Comment on the morphology of the erythrocytes.
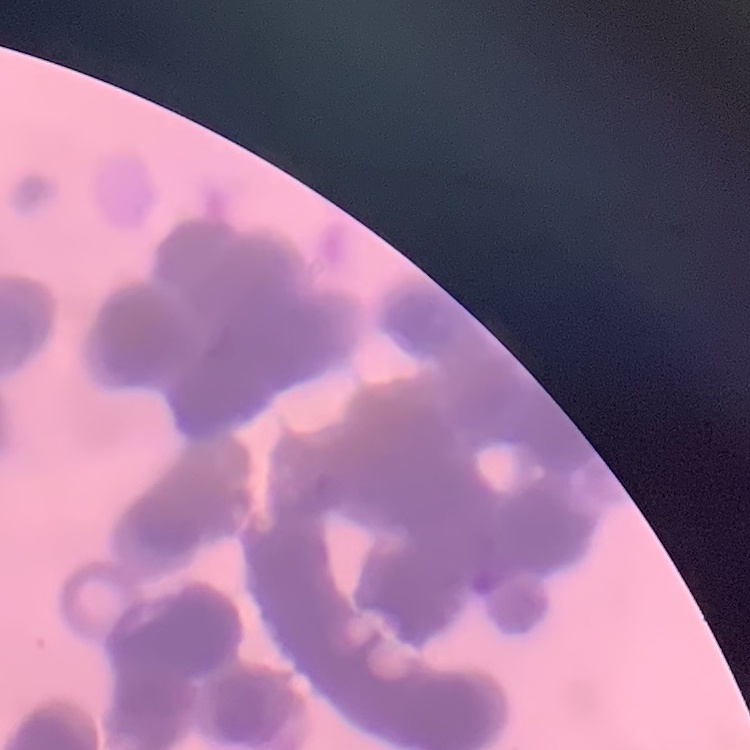
Rouleaux formation.

Thin blood film. Field's or Giemsa stain. One tile cut from a larger photomicrograph.